Classify this cell by malaria status.
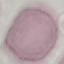

Uninfected.

image type = cell patch, automatically extracted from a larger field of view and resized to 64 × 64 pixels
capture = smartphone through the microscope eyepiece
stain = Giemsa
preparation = thin blood smear